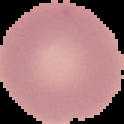

Segmented cell region on a black background. Malaria status: uninfected. From a thin blood smear. Image is 124×124 pixels.